Locate every Plasmodium parasite.
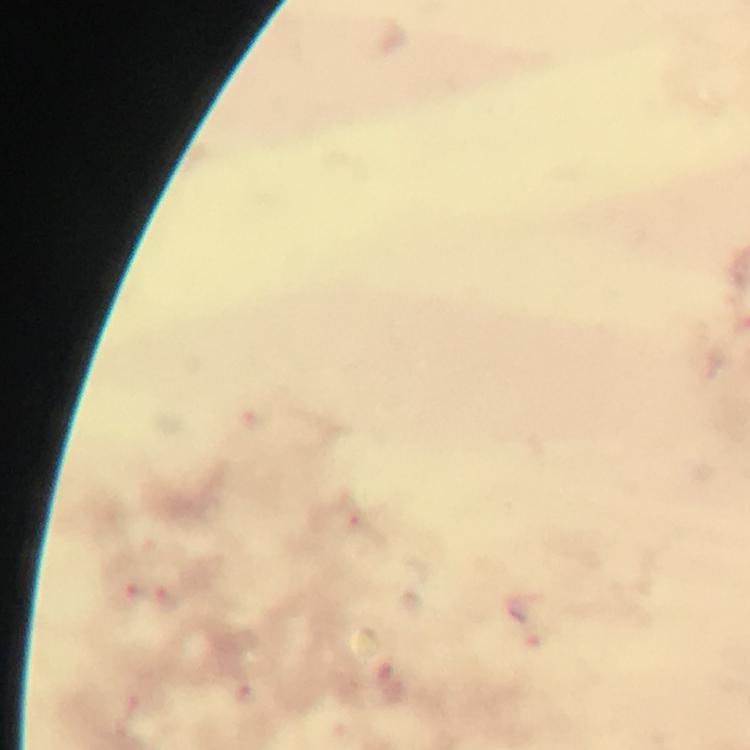
Approximate centers as [x, y] in pixels.
Plasmodium parasites: [135, 593], [169, 602].

From a malaria diagnostic workup. A crop from one field of view. Giemsa stain. 100x magnification. Immersion oil was used. Image is 750×750 pixels. Thick blood film. Photographed through the microscope with a smartphone camera.